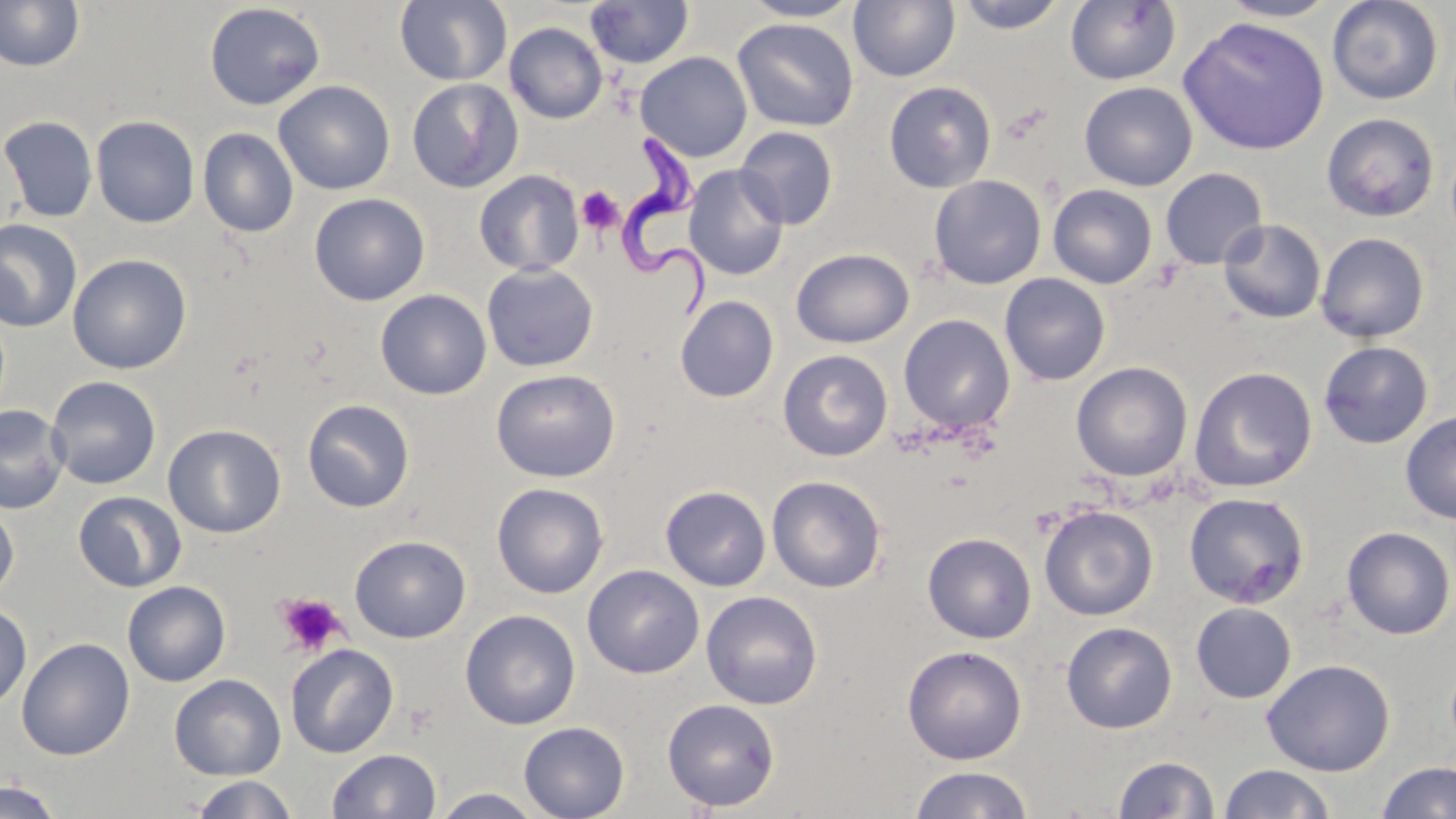

slide-level diagnosis = Trypanosoma brucei
modality = light microscopy
preparation = thin blood film
stain = May-Grünwald-Giemsa
image size = 1456×819 pixels
field of view = single
platelet locations = approximate bounding boxes as (x1,y1)-(x2,y2) corner pairs in pixels: (576,184)-(625,235), (275,592)-(348,658)
Trypanosoma brucei locations = approximate bounding boxes as (x1,y1)-(x2,y2) corner pairs in pixels: (621,133)-(724,316)
magnification = 1000x
uninfected red blood cell locations = approximate bounding boxes as (x1,y1)-(x2,y2) corner pairs in pixels: (0,0)-(85,72), (395,0)-(512,86), (739,0)-(864,22), (1218,0)-(1340,22), (1327,0)-(1444,105), (585,1)-(694,69), (848,1)-(961,83), (953,1)-(1071,34), (1065,1)-(1181,86), (204,3)-(326,110), (732,17)-(859,132), (1177,18)-(1330,156), (504,22)-(608,124), (635,52)-(753,162), (407,77)-(524,194), (273,80)-(395,195), (883,81)-(997,193), (1079,81)-(1197,191), (1321,113)-(1440,222), (0,115)-(98,223), (91,115)-(200,227), (734,125)-(839,230), (198,127)-(298,238), (683,165)-(789,281), (1160,168)-(1268,270), (473,170)-(584,277), (928,175)-(1046,288), (1047,184)-(1158,289), (309,193)-(430,306), (0,219)-(83,333), (1218,219)-(1326,324), (1316,232)-(1429,343), (791,248)-(914,348), (67,253)-(192,374), (481,263)-(599,372), (999,273)-(1110,386), (375,289)-(491,400), (674,295)-(779,402), (899,314)-(1016,435), (1318,340)-(1433,449), (777,349)-(893,462), (1070,361)-(1193,482), (1189,366)-(1317,493), (490,368)-(620,483), (46,375)-(161,490), (302,398)-(415,513), (0,405)-(70,514), (1400,411)-(1456,523), (162,424)-(286,538), (766,475)-(887,593), (491,482)-(609,599), (660,485)-(771,591), (73,491)-(187,592), (1183,492)-(1310,609), (0,502)-(19,601), (1039,504)-(1158,621), (1341,526)-(1455,639), (922,532)-(1037,643), (350,534)-(471,643), (582,564)-(704,679), (122,580)-(231,687), (701,590)-(823,710), (1191,602)-(1297,703), (0,606)-(32,710), (460,609)-(581,730), (1061,621)-(1178,734), (16,637)-(135,760), (285,643)-(398,758), (902,645)-(1027,765), (1261,659)-(1395,776), (170,674)-(286,780), (662,698)-(780,812), (518,721)-(630,819), (327,748)-(441,819), (1113,755)-(1219,818), (1377,761)-(1456,819), (1218,764)-(1337,819), (909,765)-(1034,819), (190,775)-(299,818), (0,780)-(63,819), (429,787)-(545,818)